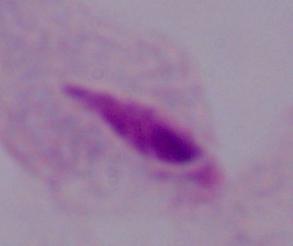
Summary:
  - Identification: trichomonad
  - Magnification: 1000x
  - Modality: micrograph